Identify the cell.
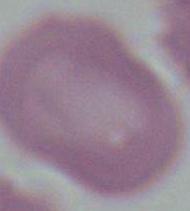

An erythrocyte.

Photomicrograph. 1000x magnification.